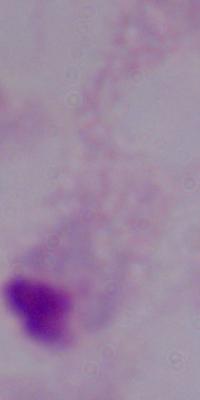
modality = photomicrograph
magnification = 1000x
identification = trichomonad